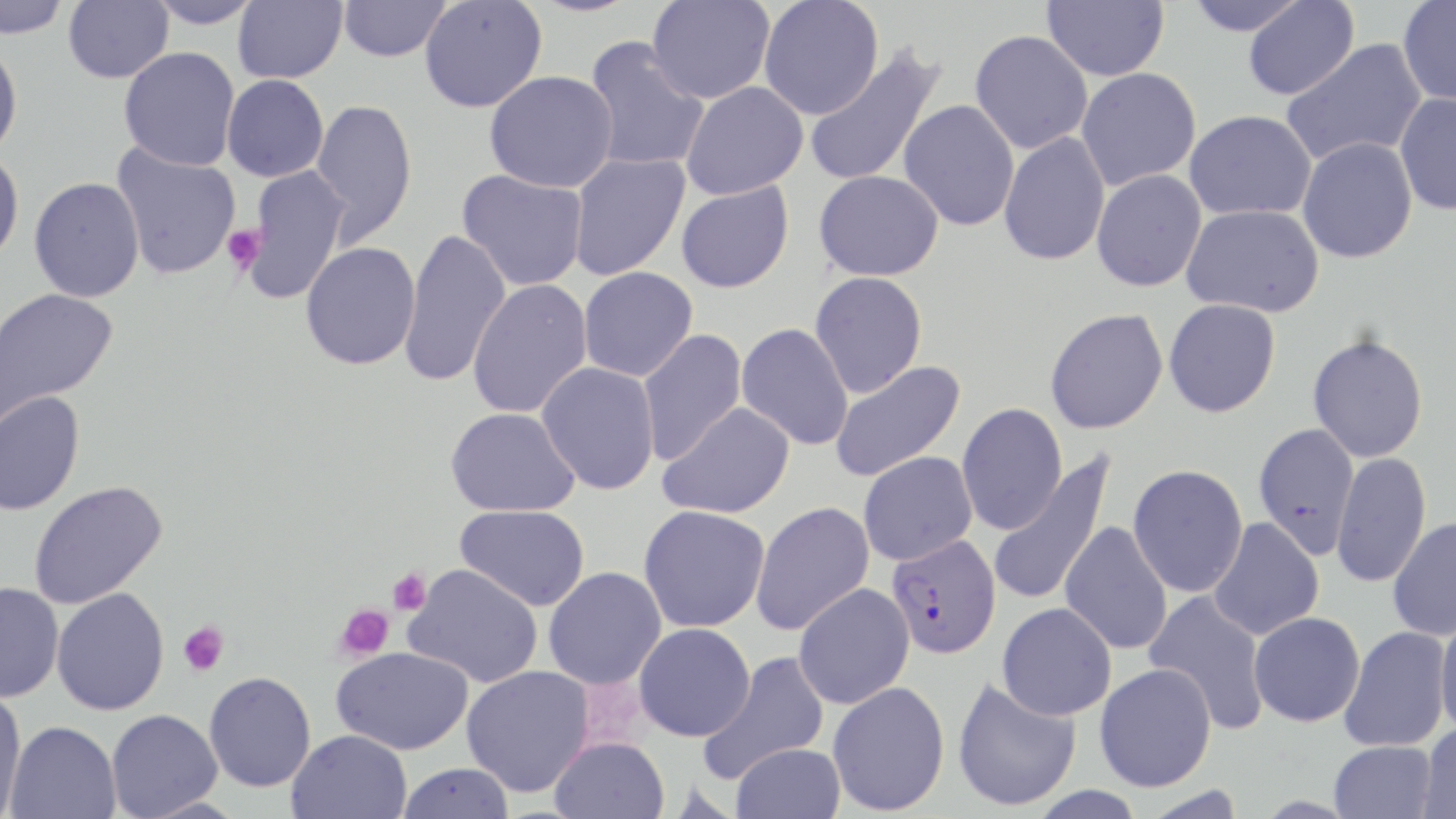
Summary:
  - Coordinate format: approximate bounding boxes as (x1, y1, x2, y2) in pixels
  - Uninfected red blood cell locations: (1, 0, 69, 38), (62, 0, 174, 84), (146, 0, 262, 28), (233, 0, 347, 84), (338, 0, 450, 62), (647, 0, 775, 104), (758, 0, 884, 120), (1042, 0, 1169, 81), (1182, 0, 1310, 36), (1397, 0, 1456, 106), (419, 1, 547, 113), (1242, 1, 1360, 101), (969, 30, 1093, 154), (582, 38, 709, 173), (0, 39, 23, 160), (1281, 39, 1428, 168), (803, 45, 947, 188), (119, 47, 240, 171), (1076, 67, 1201, 191), (484, 71, 618, 193), (222, 74, 329, 182), (680, 82, 808, 200), (1394, 92, 1456, 215), (310, 98, 418, 246), (898, 99, 1019, 232), (1184, 110, 1317, 221), (999, 131, 1111, 267), (1297, 137, 1418, 264), (111, 143, 242, 279), (0, 148, 24, 267), (568, 153, 690, 281), (241, 165, 352, 304), (456, 169, 589, 292), (814, 169, 944, 281), (1091, 169, 1207, 292), (29, 177, 145, 303), (675, 181, 794, 293), (1181, 204, 1325, 317), (399, 229, 511, 388), (300, 241, 421, 370), (579, 266, 698, 382), (810, 271, 928, 398), (467, 279, 593, 419), (0, 287, 119, 426), (1164, 299, 1281, 417), (1044, 308, 1168, 434), (736, 322, 854, 451), (637, 329, 747, 465), (1307, 334, 1429, 463), (829, 360, 966, 483), (536, 362, 660, 495), (0, 391, 85, 516), (657, 402, 795, 519), (956, 403, 1067, 535), (445, 407, 580, 517), (1252, 423, 1360, 558), (857, 452, 977, 565), (987, 452, 1117, 608), (1331, 452, 1432, 588), (1128, 465, 1248, 597), (28, 480, 167, 609), (750, 501, 876, 635), (455, 504, 590, 611), (638, 505, 770, 632), (1386, 516, 1456, 641), (1205, 518, 1321, 642), (1060, 522, 1173, 654), (404, 563, 543, 687), (543, 567, 667, 690), (0, 582, 63, 702), (793, 583, 915, 709), (51, 588, 169, 715), (1143, 590, 1271, 735), (997, 602, 1116, 720), (1249, 612, 1365, 727), (1434, 614, 1456, 737), (634, 623, 755, 741), (1339, 625, 1452, 752), (331, 646, 474, 755), (697, 651, 830, 785), (1094, 662, 1216, 791), (461, 666, 595, 798), (204, 671, 316, 792), (951, 676, 1081, 812), (827, 681, 950, 815), (0, 688, 27, 817), (105, 709, 223, 819), (5, 720, 121, 818), (1418, 723, 1456, 819), (286, 729, 412, 819), (550, 736, 670, 819), (1329, 741, 1437, 819), (731, 743, 846, 819), (396, 762, 516, 819)
  - Platelet locations: (222, 224, 266, 274), (387, 567, 432, 615), (334, 602, 395, 661), (179, 620, 230, 677)
  - Plasmodium falciparum-infected red blood cell locations: (886, 533, 1002, 659)
  - Slide-level diagnosis: Plasmodium falciparum
  - Image size: 1456×819 pixels
  - Magnification: 1000x
  - Field of view: one of a larger specimen
  - Modality: optical microscopy
  - Preparation: thin blood smear
  - Stain: May-Grünwald-Giemsa